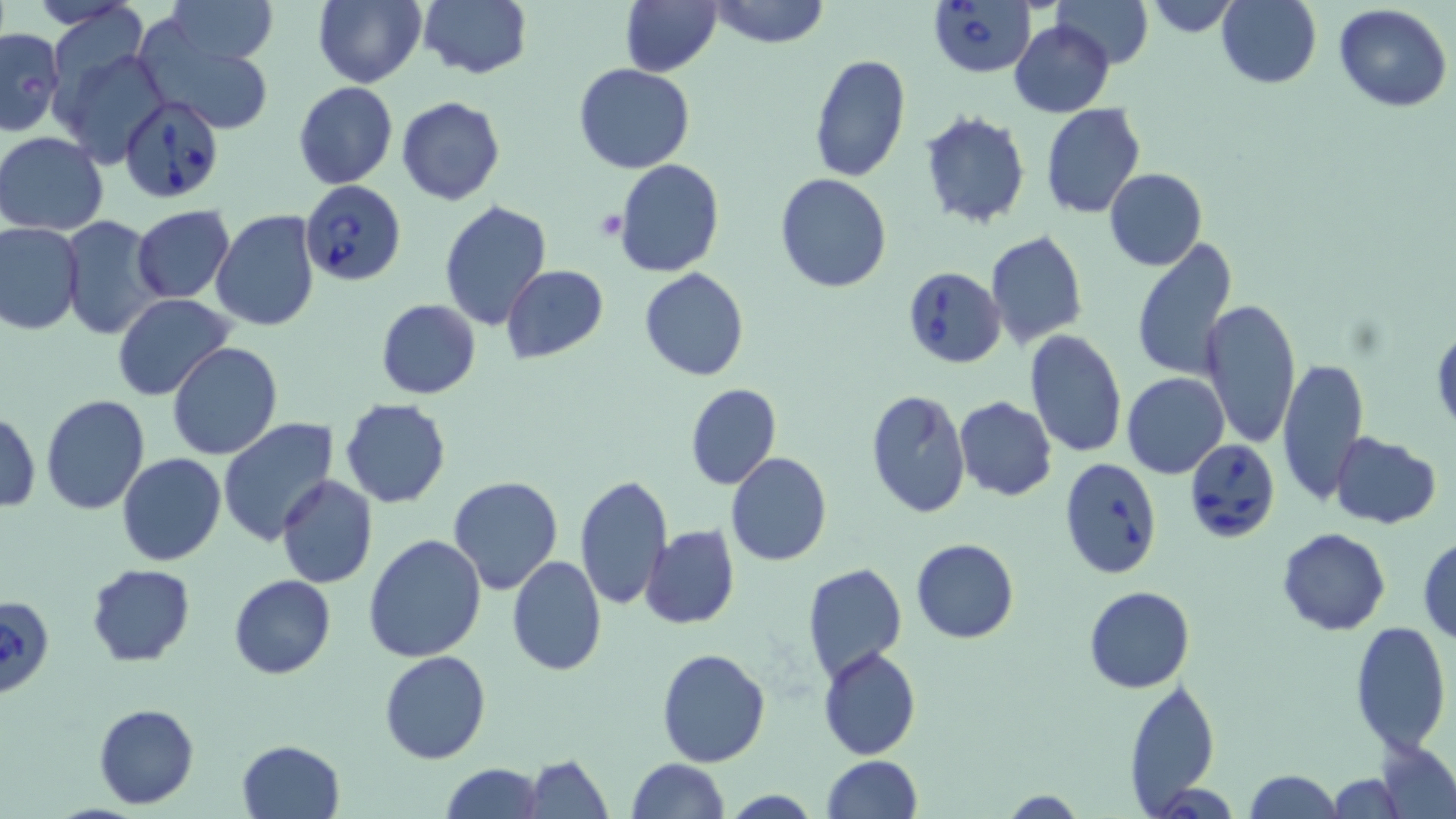
Approximate bounding boxes as [x1, y1, x2, y2] in pixels. Babesia divergens-infected red blood cell locations: [928, 0, 1036, 77], [120, 93, 226, 203], [303, 182, 406, 287], [901, 265, 1006, 367], [1183, 436, 1279, 543], [1059, 457, 1164, 580], [0, 595, 56, 700]. Uninfected red blood cell locations: [167, 0, 276, 64], [313, 0, 425, 87], [420, 0, 531, 79], [620, 0, 722, 77], [710, 0, 830, 49], [1053, 0, 1152, 68], [1144, 0, 1240, 37], [1218, 0, 1321, 88], [1333, 3, 1451, 113], [1010, 21, 1113, 117], [134, 24, 277, 136], [0, 27, 64, 136], [52, 45, 169, 169], [809, 53, 911, 183], [573, 62, 695, 173], [293, 81, 398, 190], [395, 96, 505, 205], [1042, 104, 1146, 218], [919, 109, 1031, 229], [0, 131, 111, 235], [614, 159, 725, 277], [1104, 167, 1206, 271], [776, 173, 891, 294], [438, 200, 552, 330], [131, 205, 235, 303], [210, 210, 321, 332], [59, 215, 164, 340], [0, 222, 84, 335], [986, 230, 1088, 349], [1130, 236, 1238, 381], [501, 265, 609, 364], [640, 268, 750, 381], [112, 293, 235, 402], [1199, 298, 1301, 449], [375, 299, 481, 400], [1432, 325, 1455, 438], [1022, 329, 1127, 459], [168, 343, 282, 459], [1277, 358, 1369, 506], [1122, 372, 1229, 479], [685, 383, 781, 490], [866, 389, 970, 517], [40, 394, 151, 514], [954, 396, 1057, 501], [339, 398, 451, 508], [0, 409, 41, 514], [218, 417, 339, 545], [1330, 432, 1442, 529], [116, 452, 226, 566], [726, 452, 832, 566], [574, 473, 673, 610], [447, 474, 563, 594], [276, 475, 378, 588], [641, 525, 739, 629], [1276, 528, 1391, 636], [362, 533, 488, 664], [1418, 535, 1456, 644], [910, 539, 1019, 643], [507, 556, 605, 676], [801, 562, 908, 685], [87, 564, 195, 666], [230, 573, 336, 679], [1084, 584, 1195, 693], [1347, 621, 1451, 756], [656, 646, 772, 767], [818, 647, 921, 761], [379, 650, 490, 765], [1125, 677, 1222, 812], [92, 703, 200, 809], [237, 739, 345, 819], [1377, 739, 1456, 818], [523, 754, 614, 819], [824, 756, 922, 819], [626, 759, 727, 819], [440, 763, 542, 819], [1244, 770, 1342, 818], [1327, 772, 1409, 818], [1149, 780, 1241, 818], [720, 791, 824, 819], [1000, 791, 1087, 818]. Platelet locations: [595, 209, 628, 241]. Slide-level diagnosis: Babesia divergens. Optical microscopy. May-Grünwald-Giemsa-stained preparation. Image is 1456×819 pixels. 1000x magnification. Thin blood smear. Single field of view.